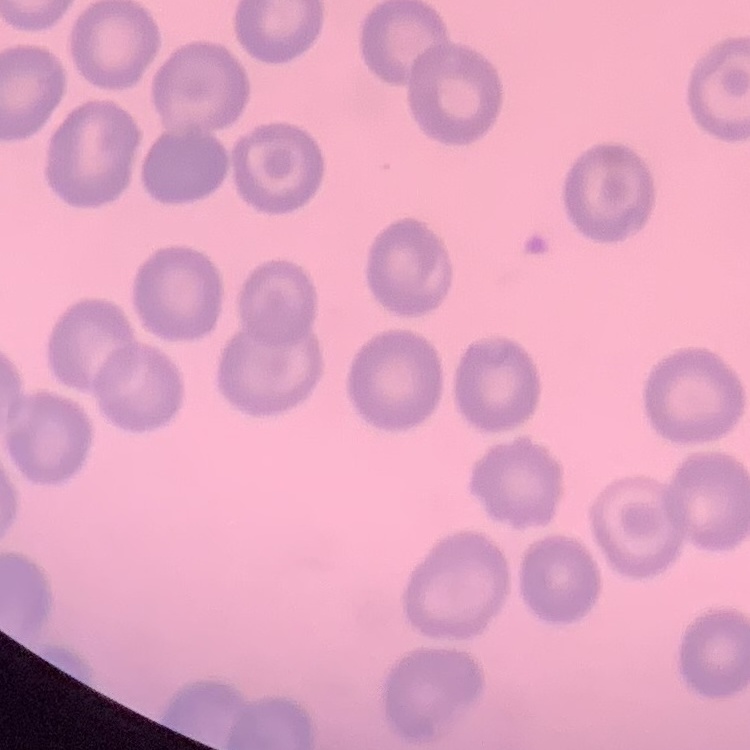

erythrocyte morphology = no rouleaux formation
image type = square crop of a larger photomicrograph
stain = Field's or Giemsa
preparation = thin blood smear